Point out each Plasmodium parasite.
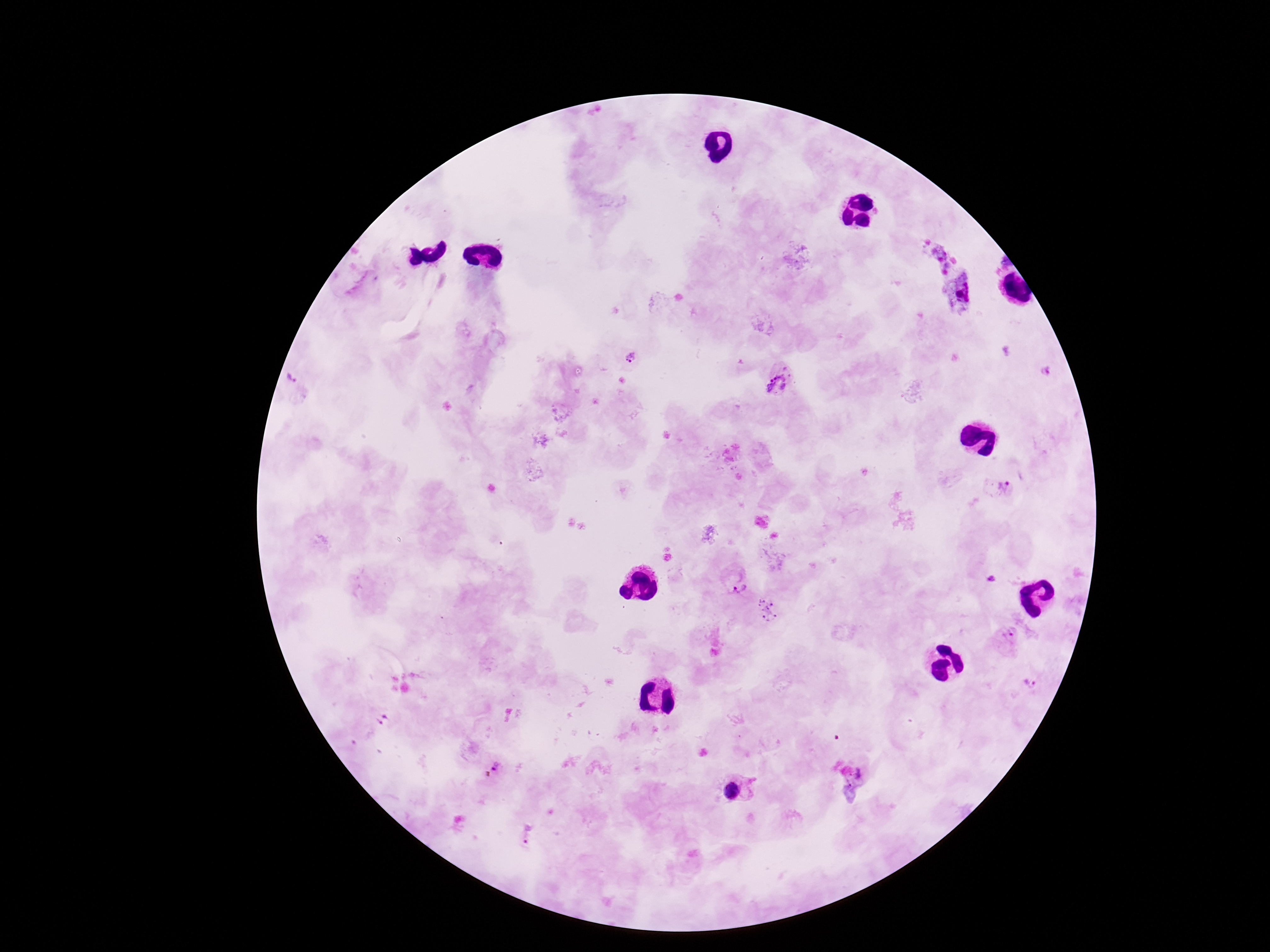

Approximate centers as [x, y] in pixels.
Plasmodium parasites: [632, 357], [1046, 370], [291, 378], [781, 381], [1000, 486], [736, 580], [765, 610], [1007, 635], [1032, 679], [497, 768], [731, 790], [528, 836].

100x magnification. Smartphone photograph taken through the microscope eyepiece. One field from this slide. Image is 1270×952 pixels. Giemsa stain. Patient malaria status: infected. Thick peripheral-blood smear.